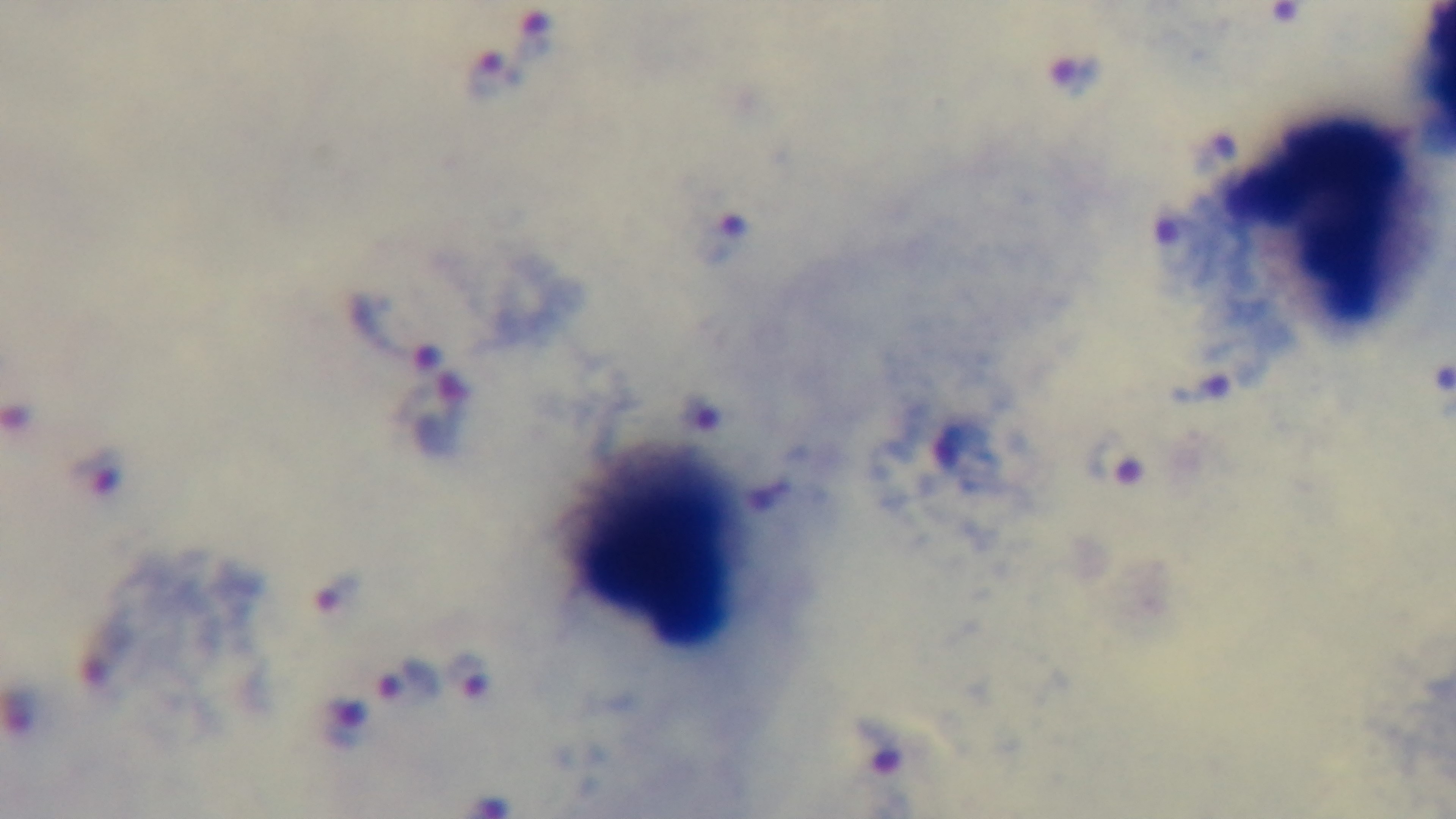
Summary:
  - Modality: light microscopy
  - Preparation: thick smear
  - Objective: 100x oil immersion
  - Field of view: single
  - Malaria status: infected
  - Capture: mounted 4K digital camera
  - Stain: Giemsa